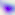 Captured at 400x magnification. Toxoplasma gondii is shown. Photomicrograph.